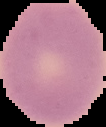

Summary:
  - Image size: 106×127 pixels
  - Image type: segmented cell region with the area outside set to black
  - Result: negative for Plasmodium parasites
  - Preparation: thin blood smear